Outline each blood parasite and name the species.
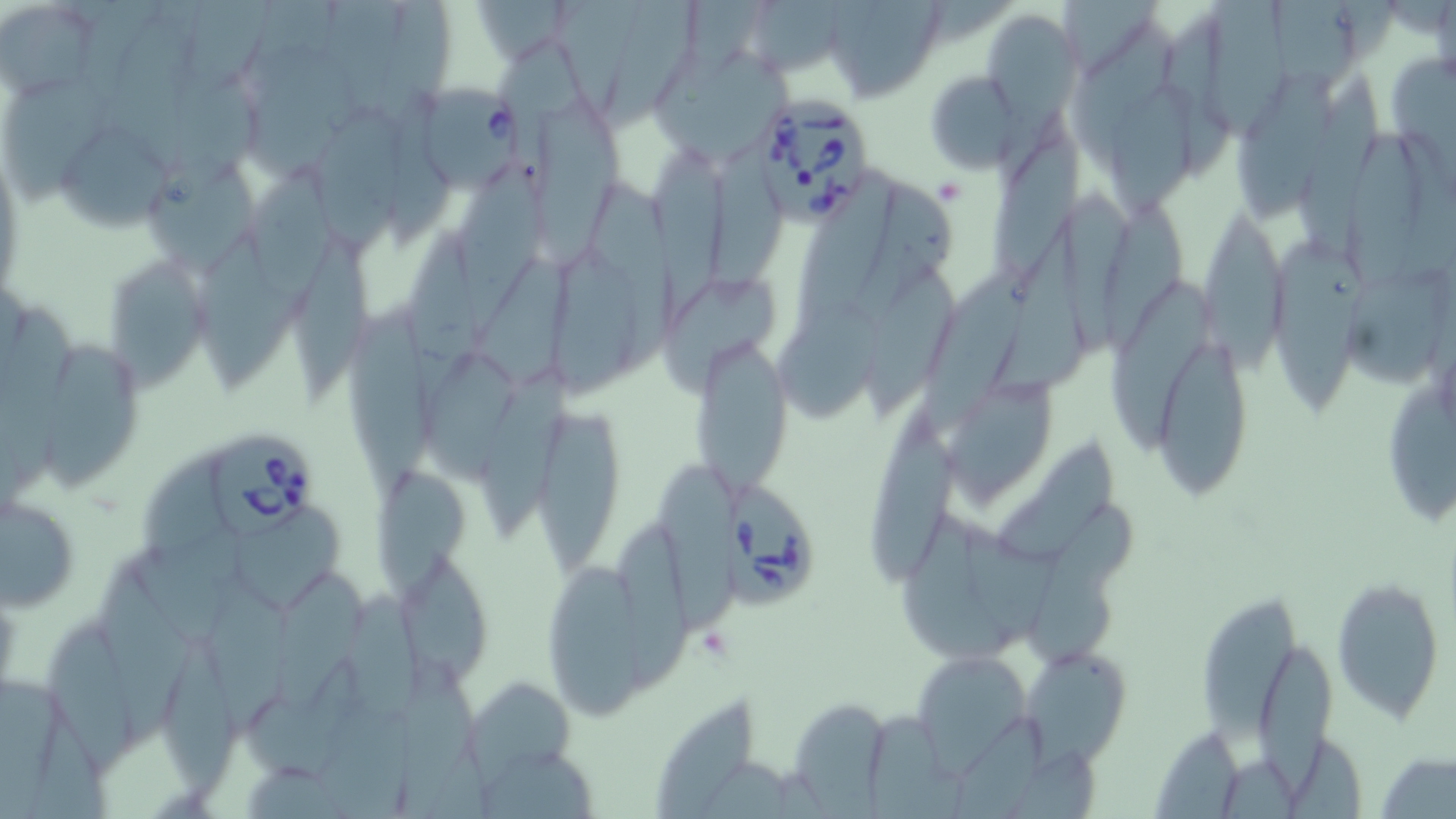

Approximate bounding boxes as (x1, y1, x2, y2) in pixels.
Babesia divergens-infected red blood cells: (421, 86, 520, 190), (743, 89, 879, 225), (211, 434, 318, 536), (720, 482, 817, 614).
No Plasmodium falciparum, Plasmodium ovale, Plasmodium malariae, Plasmodium vivax, or Trypanosoma brucei observed.

{
  "slide_level_diagnosis": "Babesia divergens",
  "platelet_locations": "approximate bounding boxes as (x1, y1, x2, y2) in pixels: (932, 178, 968, 207), (698, 625, 732, 660)",
  "magnification": "1000x",
  "preparation": "thin blood film",
  "image_size": "1456×819 pixels",
  "stain": "May-Grünwald-Giemsa",
  "modality": "optical microscopy",
  "field_of_view": "single",
  "uninfected_red_blood_cell_locations": "approximate bounding boxes as (x1, y1, x2, y2) in pixels: (80, 0, 159, 99), (186, 0, 274, 89), (253, 0, 342, 95), (475, 0, 565, 63), (553, 0, 646, 117), (610, 0, 696, 129), (688, 0, 767, 70), (821, 0, 947, 102), (1058, 1, 1162, 79), (1273, 1, 1355, 88), (384, 2, 452, 125), (1207, 2, 1287, 144), (757, 3, 847, 77), (3, 4, 98, 101), (982, 7, 1082, 116), (1158, 7, 1237, 180), (109, 13, 192, 165), (1067, 19, 1179, 163), (494, 43, 605, 135), (651, 45, 796, 163), (169, 48, 261, 190), (1393, 54, 1456, 182), (1230, 70, 1335, 218), (925, 72, 1023, 173), (1298, 73, 1387, 255), (2, 78, 110, 202), (247, 80, 350, 182), (1110, 81, 1204, 214), (392, 93, 454, 248), (536, 99, 622, 263), (316, 106, 404, 253), (53, 121, 171, 230), (1337, 126, 1425, 300), (713, 136, 789, 290), (988, 137, 1087, 281), (650, 144, 736, 330), (460, 156, 549, 347), (139, 159, 261, 278), (243, 164, 340, 325), (790, 168, 898, 337), (588, 176, 677, 384), (843, 182, 956, 335), (1061, 184, 1137, 365), (1094, 195, 1200, 356), (1197, 201, 1289, 370), (995, 219, 1091, 397), (406, 224, 487, 430), (198, 230, 302, 393), (296, 232, 373, 404), (1274, 240, 1371, 416), (555, 242, 636, 404), (476, 254, 572, 389), (110, 259, 207, 403), (1349, 262, 1449, 386), (904, 265, 1034, 439), (867, 267, 961, 430), (659, 268, 783, 403), (1107, 278, 1213, 446), (775, 297, 884, 426), (2, 301, 82, 490), (345, 303, 431, 499), (693, 330, 791, 499), (1158, 333, 1252, 493), (48, 341, 140, 497), (421, 354, 518, 484), (476, 368, 572, 542), (942, 374, 1061, 515), (1388, 383, 1456, 528), (536, 407, 625, 576), (871, 411, 960, 587), (999, 437, 1120, 557), (143, 449, 231, 556), (653, 460, 746, 631), (375, 468, 476, 595), (2, 493, 80, 611), (1025, 498, 1140, 667), (232, 510, 350, 613), (898, 513, 1011, 660), (959, 520, 1077, 646), (613, 522, 691, 690), (130, 527, 259, 648), (401, 550, 488, 682), (544, 555, 650, 722), (93, 567, 195, 739), (276, 571, 373, 716), (1332, 575, 1445, 724), (206, 579, 294, 736), (348, 587, 426, 727), (1197, 597, 1302, 744), (46, 623, 133, 774), (1256, 637, 1335, 798), (166, 643, 234, 808), (1023, 643, 1130, 763), (911, 650, 1030, 768), (394, 658, 485, 818), (247, 660, 368, 779), (0, 671, 70, 819), (463, 674, 578, 779), (316, 689, 418, 819), (653, 692, 757, 817), (792, 698, 893, 819), (866, 699, 969, 819), (31, 712, 109, 819), (955, 715, 1049, 819), (1153, 728, 1253, 819), (1290, 739, 1371, 819), (478, 745, 600, 819), (1009, 748, 1107, 819), (1378, 751, 1456, 818), (1218, 755, 1304, 819), (245, 763, 353, 819)"
}